Assess the morphology of the red blood cells.
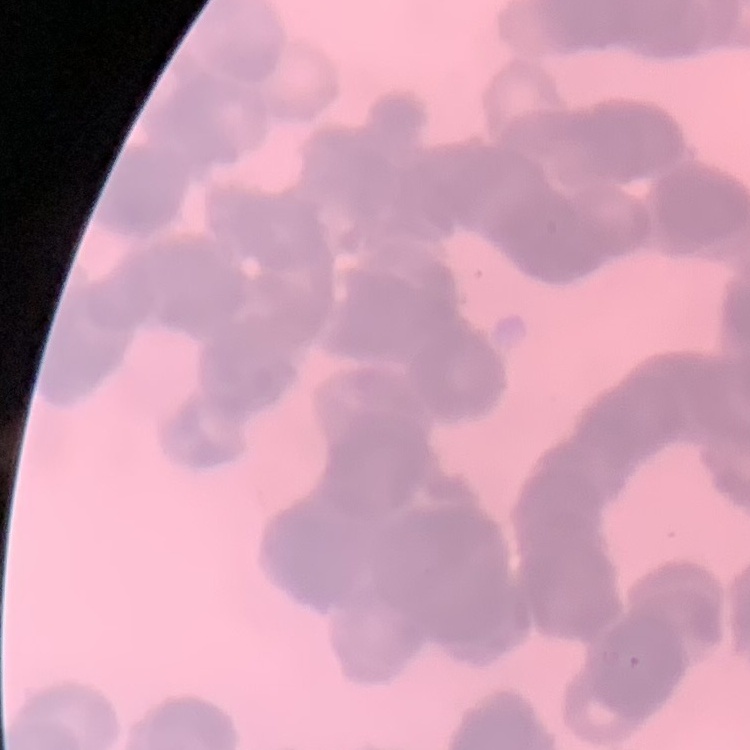
Rouleaux formation.

Summary:
  - Image type: one tile cut from a larger photomicrograph
  - Preparation: thin peripheral smear
  - Stain: Field's or Giemsa